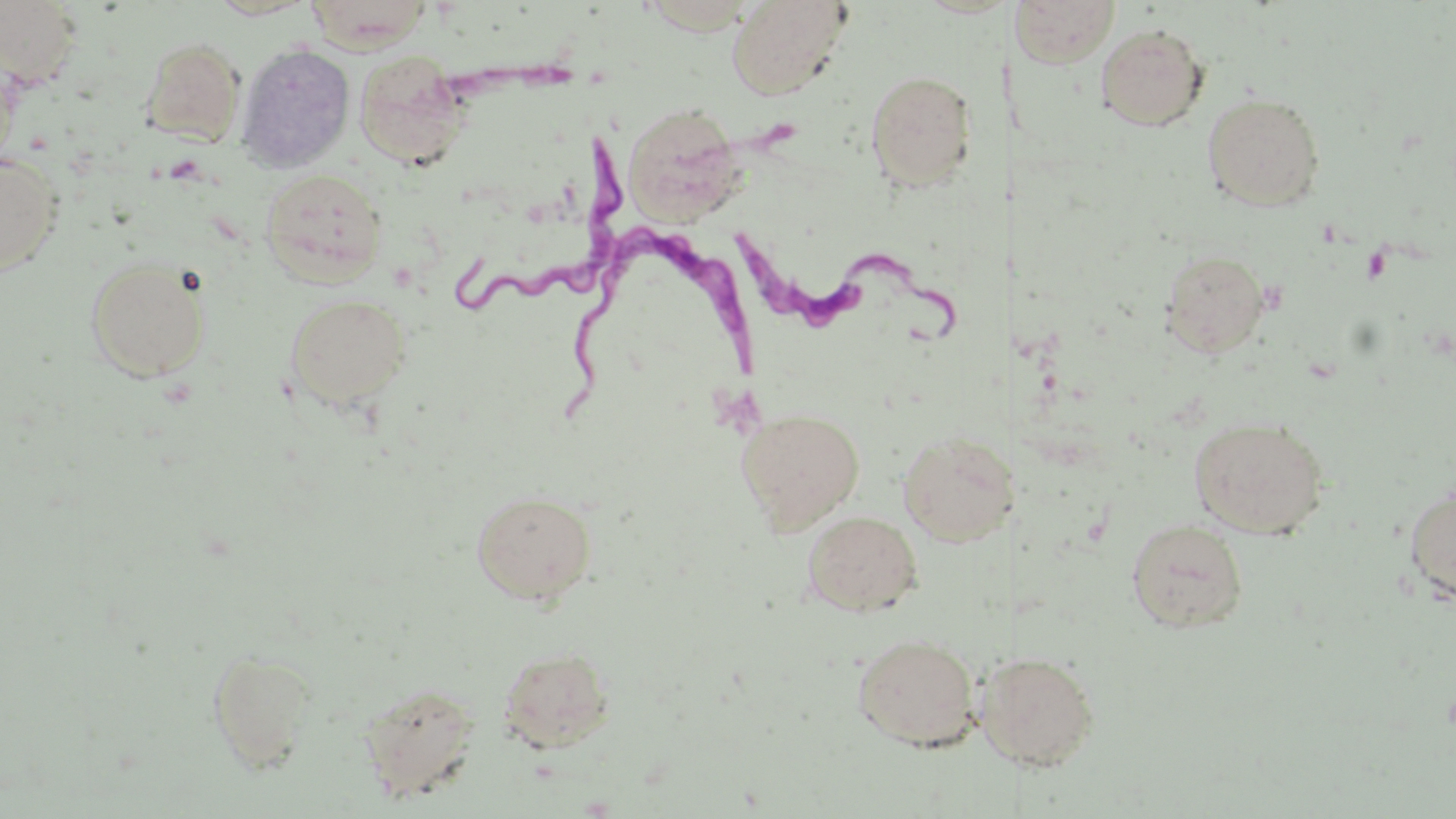
slide-level diagnosis = Trypanosoma brucei
magnification = 1000x
field of view = single
preparation = thin blood film
uninfected red blood cell locations = approximate bounding boxes as named x1/y1/x2/y2 corners in pixels: (x1=0, y1=0, x2=84, y2=87), (x1=205, y1=0, x2=319, y2=20), (x1=726, y1=0, x2=853, y2=100), (x1=1012, y1=0, x2=1121, y2=68), (x1=304, y1=1, x2=434, y2=50), (x1=1095, y1=23, x2=1210, y2=132), (x1=140, y1=37, x2=245, y2=145), (x1=236, y1=41, x2=356, y2=173), (x1=354, y1=52, x2=472, y2=171), (x1=865, y1=69, x2=978, y2=193), (x1=1202, y1=92, x2=1325, y2=211), (x1=621, y1=102, x2=746, y2=225), (x1=0, y1=152, x2=63, y2=276), (x1=260, y1=168, x2=388, y2=286), (x1=1158, y1=248, x2=1272, y2=359), (x1=85, y1=258, x2=211, y2=382), (x1=285, y1=293, x2=412, y2=409), (x1=736, y1=407, x2=865, y2=533), (x1=1189, y1=416, x2=1329, y2=539), (x1=897, y1=429, x2=1010, y2=546), (x1=1404, y1=482, x2=1456, y2=606), (x1=470, y1=489, x2=597, y2=604), (x1=801, y1=510, x2=924, y2=617), (x1=1126, y1=519, x2=1248, y2=633), (x1=852, y1=632, x2=981, y2=750), (x1=497, y1=646, x2=616, y2=753), (x1=207, y1=648, x2=318, y2=772), (x1=996, y1=651, x2=1100, y2=771), (x1=358, y1=681, x2=483, y2=803)
Trypanosoma brucei locations = approximate bounding boxes as named x1/y1/x2/y2 corners in pixels: (x1=454, y1=112, x2=634, y2=324), (x1=739, y1=223, x2=977, y2=351), (x1=567, y1=236, x2=767, y2=415)
stain = May-Grünwald-Giemsa
modality = optical microscopy
image size = 1456×819 pixels